Locate and identify every blood parasite.
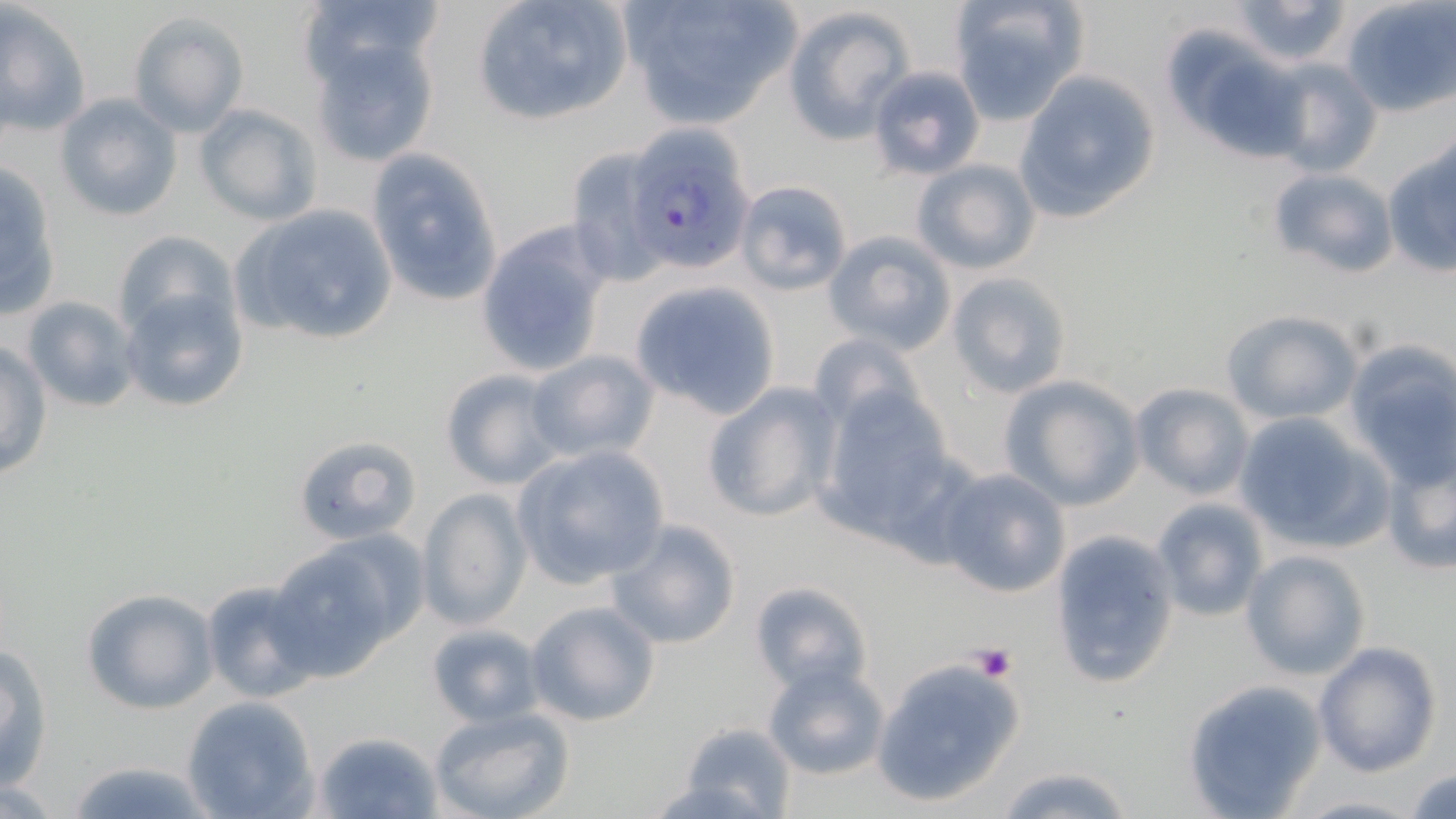
Approximate bounding boxes as named x1/y1/x2/y2 corners in pixels.
Plasmodium falciparum-infected red blood cells: (x1=624, y1=122, x2=760, y2=276).
No Plasmodium ovale, Plasmodium malariae, Plasmodium vivax, Babesia divergens, or Trypanosoma brucei observed.

slide-level diagnosis = Plasmodium falciparum
preparation = thin blood smear
platelet locations = approximate bounding boxes as named x1/y1/x2/y2 corners in pixels: (x1=972, y1=642, x2=1017, y2=681)
image size = 1456×819 pixels
field of view = single
modality = optical microscopy
uninfected red blood cell locations = approximate bounding boxes as named x1/y1/x2/y2 corners in pixels: (x1=297, y1=0, x2=447, y2=85), (x1=469, y1=0, x2=637, y2=127), (x1=616, y1=0, x2=808, y2=128), (x1=948, y1=0, x2=1088, y2=124), (x1=1228, y1=0, x2=1354, y2=66), (x1=1342, y1=0, x2=1456, y2=116), (x1=0, y1=2, x2=91, y2=138), (x1=781, y1=5, x2=916, y2=143), (x1=128, y1=12, x2=249, y2=136), (x1=1160, y1=23, x2=1299, y2=160), (x1=308, y1=31, x2=443, y2=172), (x1=1265, y1=58, x2=1383, y2=178), (x1=865, y1=66, x2=985, y2=180), (x1=1013, y1=70, x2=1160, y2=222), (x1=55, y1=93, x2=183, y2=221), (x1=191, y1=103, x2=323, y2=225), (x1=1382, y1=141, x2=1455, y2=276), (x1=364, y1=146, x2=503, y2=310), (x1=564, y1=146, x2=675, y2=285), (x1=909, y1=158, x2=1041, y2=276), (x1=0, y1=159, x2=63, y2=320), (x1=1266, y1=167, x2=1399, y2=279), (x1=732, y1=179, x2=854, y2=296), (x1=230, y1=204, x2=400, y2=348), (x1=476, y1=221, x2=614, y2=378), (x1=109, y1=229, x2=236, y2=345), (x1=824, y1=230, x2=957, y2=353), (x1=946, y1=271, x2=1073, y2=399), (x1=631, y1=280, x2=781, y2=419), (x1=118, y1=284, x2=249, y2=414), (x1=20, y1=296, x2=142, y2=412), (x1=1221, y1=309, x2=1363, y2=424), (x1=808, y1=330, x2=931, y2=434), (x1=1, y1=339, x2=52, y2=483), (x1=1344, y1=342, x2=1456, y2=484), (x1=524, y1=350, x2=661, y2=465), (x1=439, y1=368, x2=566, y2=491), (x1=998, y1=375, x2=1145, y2=512), (x1=701, y1=381, x2=842, y2=524), (x1=1129, y1=381, x2=1255, y2=500), (x1=809, y1=383, x2=963, y2=543), (x1=1232, y1=411, x2=1392, y2=553), (x1=291, y1=432, x2=423, y2=546), (x1=510, y1=445, x2=670, y2=589), (x1=1380, y1=447, x2=1456, y2=576), (x1=937, y1=467, x2=1070, y2=597), (x1=415, y1=488, x2=531, y2=630), (x1=1151, y1=497, x2=1269, y2=621), (x1=605, y1=517, x2=742, y2=649), (x1=1048, y1=530, x2=1180, y2=689), (x1=267, y1=542, x2=410, y2=679), (x1=1239, y1=549, x2=1371, y2=681), (x1=199, y1=575, x2=327, y2=704), (x1=749, y1=580, x2=873, y2=697), (x1=80, y1=588, x2=219, y2=713), (x1=525, y1=600, x2=661, y2=726), (x1=425, y1=622, x2=546, y2=728), (x1=1, y1=639, x2=55, y2=791), (x1=1313, y1=641, x2=1442, y2=777), (x1=870, y1=654, x2=1027, y2=808), (x1=762, y1=660, x2=891, y2=782), (x1=1182, y1=678, x2=1327, y2=816), (x1=179, y1=696, x2=319, y2=819), (x1=427, y1=707, x2=576, y2=819), (x1=671, y1=723, x2=798, y2=817), (x1=314, y1=729, x2=444, y2=819), (x1=59, y1=759, x2=217, y2=818), (x1=994, y1=762, x2=1137, y2=819), (x1=1407, y1=767, x2=1456, y2=818), (x1=1289, y1=794, x2=1428, y2=818)
magnification = 1000x
stain = May-Grünwald-Giemsa